Locate and identify every blood parasite.
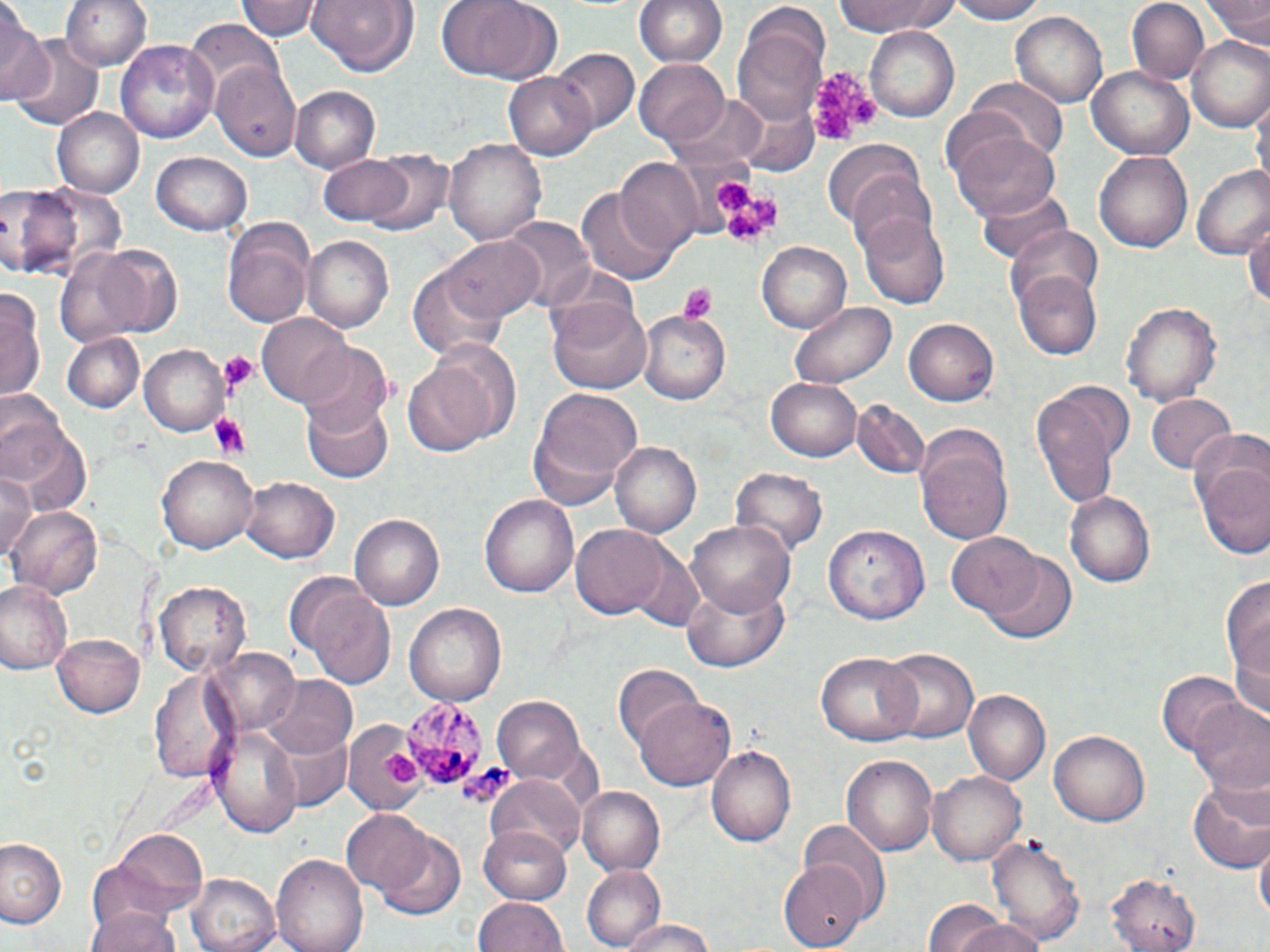

Approximate bounding boxes as (x1,y1)-(x2,y2) corner pairs in pixels.
Plasmodium malariae-infected red blood cells: (403,697)-(487,788).
No Plasmodium falciparum, Plasmodium ovale, Plasmodium vivax, Babesia divergens, or Trypanosoma brucei observed.

Platelet locations: (808,60)-(880,143), (714,180)-(751,211), (744,197)-(784,227), (724,210)-(767,243), (677,284)-(718,323), (217,351)-(258,394), (207,414)-(249,460), (380,752)-(421,789), (456,767)-(517,810). Uninfected red blood cell locations: (61,0)-(149,70), (237,0)-(319,42), (306,0)-(420,76), (436,0)-(562,82), (636,0)-(726,69), (832,0)-(962,37), (947,0)-(1046,24), (1125,0)-(1210,87), (1204,0)-(1270,48), (0,9)-(51,109), (1011,11)-(1105,109), (736,16)-(827,122), (186,22)-(282,98), (864,26)-(960,123), (1188,37)-(1270,133), (115,38)-(218,147), (10,39)-(102,131), (550,48)-(639,133), (635,59)-(732,145), (211,61)-(304,165), (1086,63)-(1195,160), (504,71)-(598,160), (969,77)-(1068,166), (293,85)-(382,171), (1254,92)-(1269,191), (730,94)-(821,178), (54,107)-(143,197), (954,130)-(1060,224), (446,139)-(546,244), (826,140)-(927,232), (1093,149)-(1197,254), (364,150)-(451,236), (153,154)-(250,237), (318,154)-(420,230), (617,157)-(704,252), (1192,166)-(1270,261), (845,173)-(940,261), (2,184)-(81,279), (578,185)-(680,285), (976,187)-(1072,269), (861,212)-(950,308), (1244,215)-(1270,315), (501,218)-(593,314), (222,219)-(313,326), (1004,225)-(1104,314), (441,234)-(542,324), (302,235)-(395,335), (757,241)-(852,333), (58,242)-(175,344), (407,263)-(507,365), (1012,269)-(1102,360), (2,285)-(44,405), (545,295)-(652,399), (1121,299)-(1222,404), (790,301)-(894,387), (639,311)-(730,403), (259,313)-(355,406), (904,319)-(1000,405), (60,331)-(145,412), (298,342)-(394,436), (139,345)-(229,435), (401,354)-(502,460), (768,377)-(862,460), (525,388)-(642,511), (1031,393)-(1122,512), (1149,394)-(1237,474), (301,395)-(397,484), (851,401)-(931,479), (0,403)-(91,517), (914,426)-(1013,547), (1187,429)-(1270,560), (611,441)-(702,539), (161,455)-(257,554), (732,467)-(828,561), (1,470)-(37,567), (241,476)-(340,565), (1064,489)-(1155,587), (481,494)-(578,597), (8,505)-(102,599), (352,513)-(447,610), (687,519)-(796,620), (826,522)-(931,621), (569,526)-(677,621), (947,533)-(1041,621), (980,552)-(1077,643), (0,578)-(75,675), (682,578)-(790,673), (1224,578)-(1270,699), (155,579)-(250,677), (303,584)-(397,687), (402,602)-(505,705), (53,633)-(146,717), (877,646)-(978,745), (206,647)-(302,737), (815,652)-(921,747), (614,665)-(703,754), (149,668)-(236,782), (1157,671)-(1244,756), (261,675)-(357,760), (964,690)-(1051,786), (634,694)-(736,793), (492,696)-(587,786), (1190,702)-(1270,799), (346,723)-(426,817), (211,725)-(303,836), (269,729)-(349,813), (1051,731)-(1150,825), (707,744)-(796,847), (842,753)-(940,857), (928,770)-(1024,866), (485,775)-(588,869), (1187,779)-(1270,873), (580,785)-(666,875), (341,810)-(433,896), (799,820)-(891,916), (481,825)-(576,906), (106,827)-(209,915), (375,831)-(466,918), (989,834)-(1084,948), (0,836)-(66,930), (1256,840)-(1269,931), (271,852)-(368,952), (778,861)-(868,947), (581,868)-(665,949), (1108,870)-(1200,951), (187,872)-(280,952), (473,897)-(570,952), (924,903)-(1043,952), (87,905)-(185,952), (620,918)-(721,952). Slide-level diagnosis: Plasmodium malariae. Optical microscopy. Thin blood smear. Image is 1270×952 pixels. 1000x magnification. One field of a larger specimen. May-Grünwald-Giemsa-stained preparation.